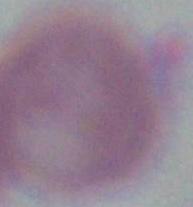
magnification = 1000x
identification = red blood cell
modality = photomicrograph